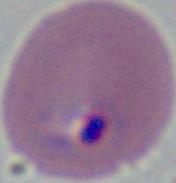

magnification = 400x or 1000x
modality = photomicrograph
identification = Plasmodium